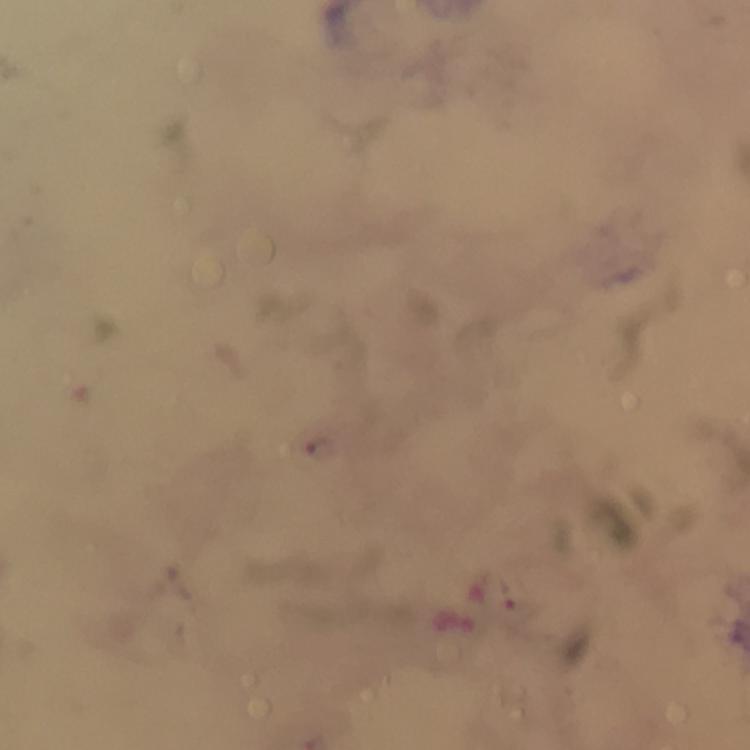

Approximate object centers, in pixels from the top-left corner. Plasmodium parasite locations: (x=321, y=447). Photographed through the microscope with a smartphone camera. At 100x magnification. Image is 750×750 pixels. Giemsa stain. Thick blood film. From a malaria diagnostic workup. A crop from one field of view. Immersion oil applied.